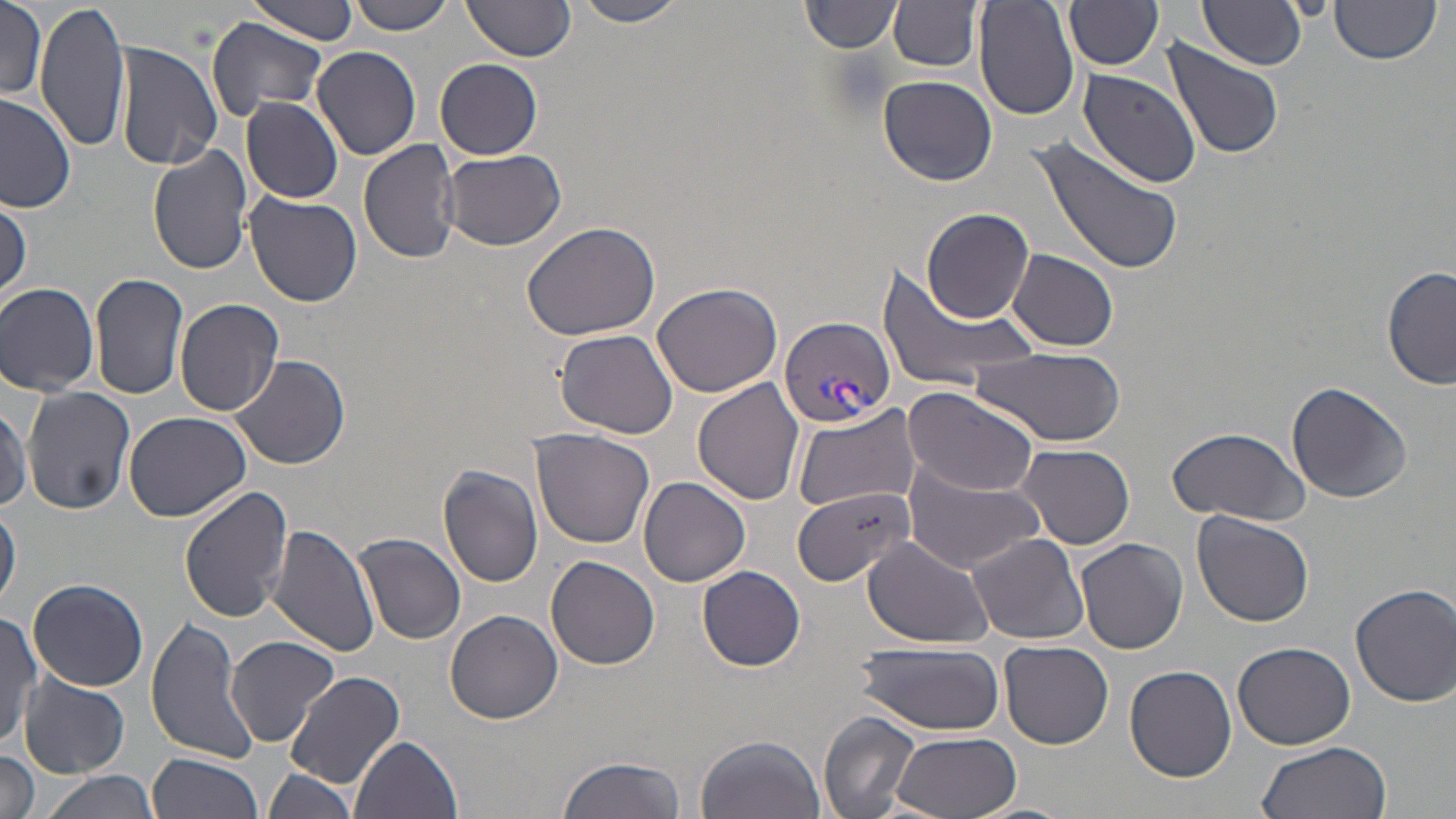

slide_level_diagnosis: Plasmodium vivax
stain: May-Grünwald-Giemsa
modality: optical microscopy
magnification: 1000x
field_of_view: one of a larger specimen
preparation: thin blood film
image_size: 1456×819 pixels
plasmodium_vivax_infected_red_blood_cell_locations: 'approximate bounding boxes as [x1, y1, x2, y2] in pixels: [778, 317, 895, 429]'
uninfected_red_blood_cell_locations: 'approximate bounding boxes as [x1, y1, x2, y2] in pixels: [35, 0, 132, 154], [243, 0, 361, 43], [349, 0, 455, 35], [571, 0, 688, 27], [803, 1, 904, 54], [973, 1, 1080, 121], [1065, 1, 1165, 71], [1199, 1, 1308, 71], [461, 2, 577, 66], [888, 2, 982, 73], [1330, 2, 1440, 66], [0, 3, 48, 99], [205, 16, 328, 123], [1161, 38, 1284, 160], [112, 39, 223, 171], [312, 47, 422, 162], [435, 58, 543, 159], [1075, 67, 1204, 187], [879, 74, 996, 185], [0, 90, 76, 215], [239, 96, 344, 202], [1029, 135, 1187, 276], [358, 138, 464, 265], [148, 144, 252, 276], [440, 149, 567, 251], [243, 191, 364, 309], [0, 197, 29, 306], [923, 208, 1033, 323], [520, 218, 663, 341], [1009, 248, 1120, 351], [1383, 266, 1455, 392], [875, 267, 1040, 395], [90, 272, 188, 401], [0, 282, 100, 395], [651, 283, 785, 398], [174, 299, 285, 418], [661, 319, 794, 495], [554, 329, 679, 439], [973, 345, 1127, 448], [231, 353, 351, 469], [695, 378, 805, 505], [1285, 381, 1412, 504], [902, 385, 1043, 495], [23, 387, 136, 515], [0, 400, 31, 515], [792, 404, 920, 513], [124, 412, 254, 524], [1166, 425, 1311, 526], [530, 430, 656, 549], [1017, 442, 1134, 550], [902, 456, 1049, 574], [437, 464, 546, 588], [639, 476, 751, 587], [179, 484, 294, 622], [789, 487, 915, 585], [0, 500, 21, 615], [1192, 510, 1314, 627], [267, 523, 380, 658], [354, 532, 466, 645], [967, 532, 1089, 644], [862, 537, 993, 647], [1076, 537, 1188, 654], [546, 555, 660, 670], [698, 565, 806, 671], [27, 577, 149, 691], [1351, 583, 1456, 706], [445, 608, 564, 723], [0, 611, 39, 749], [145, 613, 261, 764], [226, 634, 338, 745], [1000, 640, 1113, 749], [854, 641, 1008, 734], [1233, 642, 1357, 750], [1124, 664, 1237, 782], [285, 669, 406, 791], [20, 673, 129, 777], [819, 711, 921, 819], [887, 731, 1024, 819], [696, 733, 827, 819], [352, 735, 465, 819], [1256, 742, 1390, 819], [0, 750, 41, 819], [147, 753, 265, 819], [556, 755, 688, 819], [261, 768, 361, 815], [37, 771, 158, 819]'